Identify the parasite.
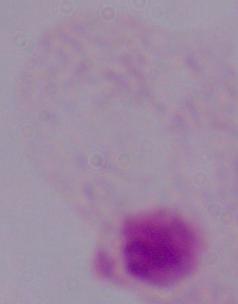
This is a trichomonad.

Summary:
  - Modality: photomicrograph
  - Magnification: 1000x